Assess this cell for malaria.
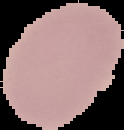
Uninfected.

Image is 124×130 pixels. Cell region segmented out of the field of view; the surrounding area is masked to black. From a thin blood film.